Locate every blood parasite and identify its species.
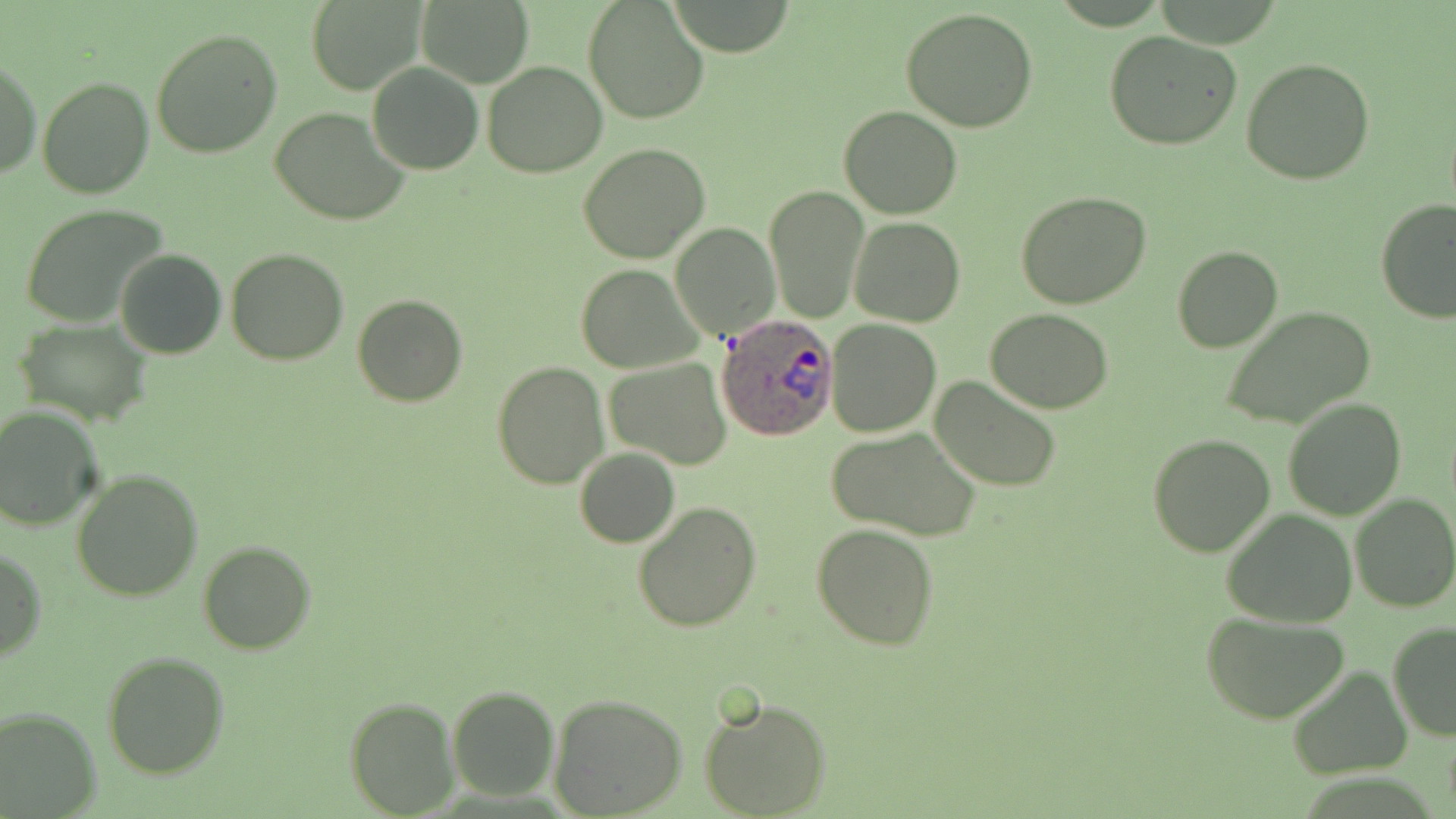
Approximate bounding boxes as (x1, y1, x2, y2) in pixels.
Plasmodium ovale-infected red blood cells: (717, 315, 837, 439).
No Plasmodium falciparum, Plasmodium malariae, Plasmodium vivax, Babesia divergens, or Trypanosoma brucei observed.

Uninfected red blood cell locations: (307, 0, 426, 95), (582, 0, 710, 122), (668, 0, 799, 57), (417, 2, 532, 85), (901, 8, 1040, 132), (150, 27, 282, 159), (1104, 31, 1242, 150), (1241, 57, 1376, 187), (1, 58, 41, 180), (482, 61, 608, 176), (366, 63, 483, 176), (36, 75, 154, 199), (839, 105, 963, 220), (269, 107, 410, 227), (578, 144, 712, 264), (763, 182, 869, 324), (1015, 191, 1153, 310), (1375, 200, 1456, 322), (18, 203, 170, 328), (848, 216, 965, 328), (669, 222, 780, 339), (1171, 245, 1283, 353), (224, 247, 348, 365), (115, 249, 227, 360), (575, 263, 702, 373), (351, 293, 468, 407), (1218, 306, 1376, 431), (985, 309, 1115, 413), (12, 320, 153, 424), (825, 320, 942, 438), (604, 357, 733, 470), (493, 361, 607, 488), (931, 376, 1062, 492), (1282, 397, 1405, 520), (0, 406, 105, 531), (825, 429, 981, 541), (1148, 432, 1277, 557), (574, 447, 680, 548), (72, 467, 203, 601), (1350, 493, 1456, 613), (633, 501, 762, 631), (1222, 510, 1358, 626), (811, 524, 939, 650), (197, 539, 317, 655), (0, 546, 45, 666), (1202, 612, 1348, 724), (1387, 621, 1456, 742), (103, 651, 232, 778), (1288, 666, 1410, 779), (447, 685, 559, 802), (548, 694, 688, 818), (343, 696, 460, 817), (699, 696, 831, 819), (0, 706, 101, 815). Slide-level diagnosis: Plasmodium ovale. 1000x magnification. May-Grünwald-Giemsa stain. Image is 1456×819 pixels. One field of a larger specimen. Thin blood film. Light microscopy.